Locate every blood parasite and identify its species.
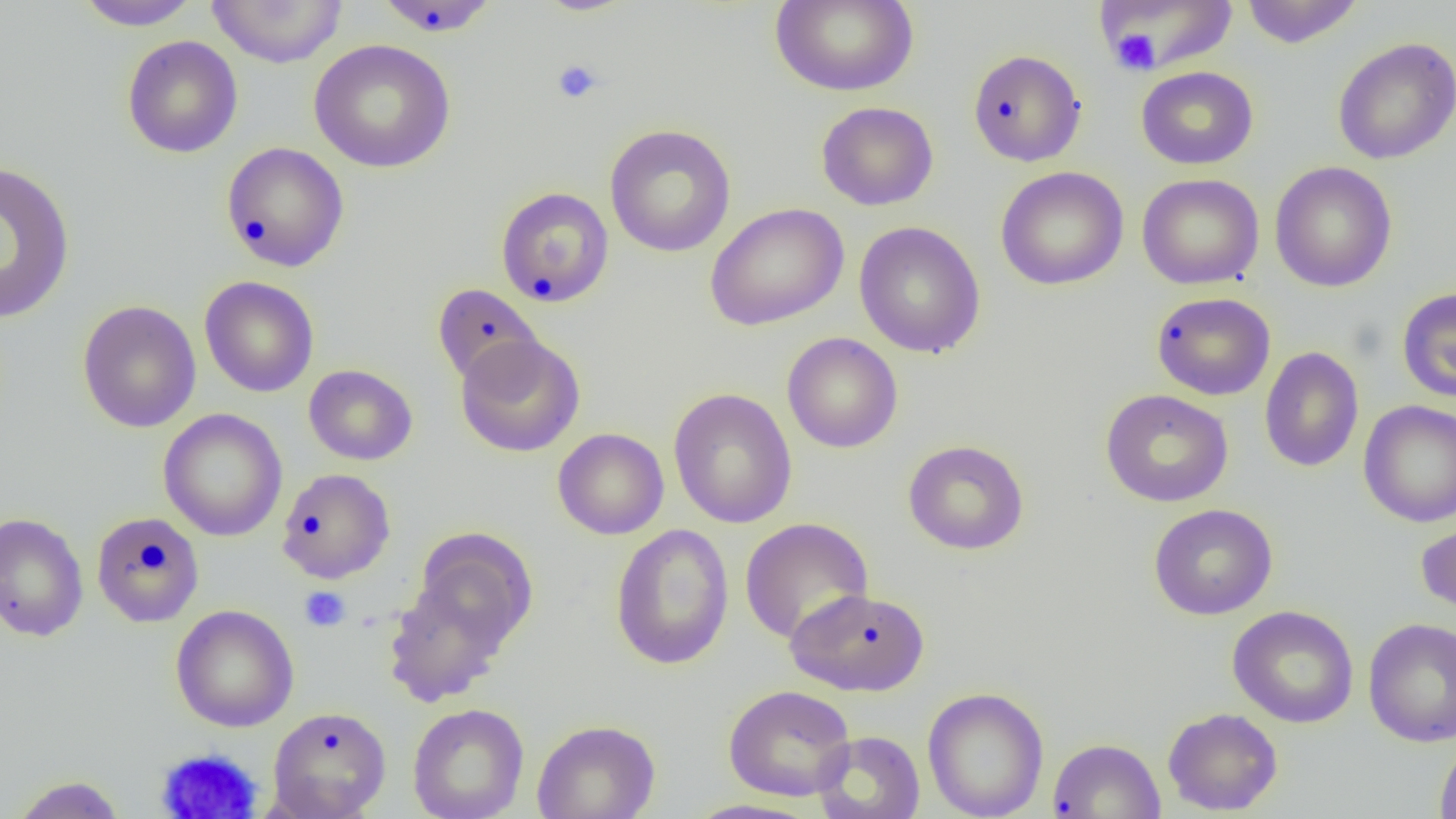

No blood parasites seen.

Summary:
  - Coordinate format: approximate bounding boxes as [x1, y1, x2, y2] in pixels
  - Platelet locations: [1110, 28, 1161, 76], [552, 59, 604, 105], [299, 586, 351, 632], [156, 747, 263, 819]
  - Uninfected red blood cell locations: [73, 0, 200, 30], [207, 0, 346, 68], [770, 0, 919, 97], [1241, 0, 1363, 48], [372, 1, 501, 37], [1094, 1, 1238, 74], [122, 35, 243, 159], [1332, 36, 1455, 165], [308, 38, 456, 173], [967, 48, 1087, 167], [1136, 66, 1258, 170], [816, 101, 938, 211], [604, 124, 736, 257], [221, 141, 349, 272], [0, 160, 76, 325], [1269, 161, 1397, 293], [995, 166, 1129, 291], [1136, 173, 1264, 290], [495, 186, 614, 308], [704, 202, 849, 331], [854, 221, 986, 358], [199, 276, 319, 397], [432, 283, 543, 387], [1397, 287, 1456, 402], [1151, 291, 1276, 401], [77, 300, 202, 433], [782, 332, 903, 453], [455, 334, 585, 457], [1259, 346, 1364, 473], [303, 364, 418, 465], [668, 388, 797, 529], [1100, 388, 1234, 507], [1359, 399, 1456, 527], [158, 408, 287, 541], [553, 427, 669, 539], [902, 439, 1030, 556], [277, 468, 395, 584], [1148, 503, 1278, 621], [0, 512, 89, 642], [91, 512, 206, 628], [1416, 516, 1456, 619], [739, 517, 874, 645], [610, 523, 735, 670], [413, 529, 538, 655], [382, 573, 514, 707], [786, 587, 930, 697], [171, 604, 299, 732], [1227, 605, 1359, 728], [1363, 617, 1456, 746], [723, 684, 856, 802], [922, 686, 1050, 819], [408, 703, 529, 819], [267, 705, 392, 818], [1162, 707, 1284, 816], [532, 719, 661, 819], [812, 730, 926, 819], [1047, 737, 1165, 818], [1434, 738, 1456, 819], [7, 775, 128, 818], [682, 799, 822, 819]
  - Slide-level diagnosis: negative for blood parasites
  - Field of view: single
  - Modality: light microscopy
  - Image size: 1456×819 pixels
  - Magnification: 1000x
  - Preparation: thin blood smear